Name the cell type shown.
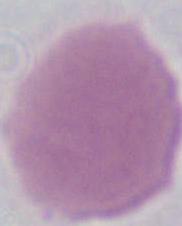

This is an erythrocyte.

1000x magnification. Photomicrograph.